Report the malaria status of this cell.
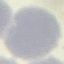

Uninfected.

Summary:
  - Preparation: thin blood smear
  - Stain: Giemsa
  - Image type: automatically extracted cell patch, resized to 64 × 64 pixels
  - Capture: smartphone camera at the microscope eyepiece